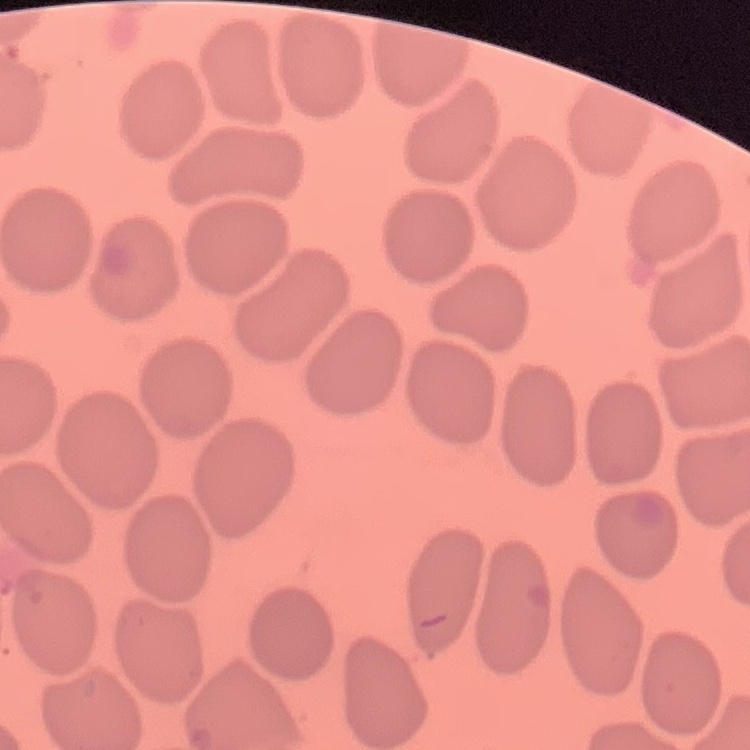
red blood cell morphology = no rouleaux formation
image type = square crop of a larger photomicrograph
preparation = thin peripheral smear
stain = Field's or Giemsa